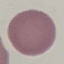
result = negative for malaria parasites
image type = cell patch, automatically extracted from a larger field of view and resized to 64 × 64 pixels
preparation = thin smear
capture = smartphone through the microscope eyepiece
stain = Giemsa